State the blood parasite species.
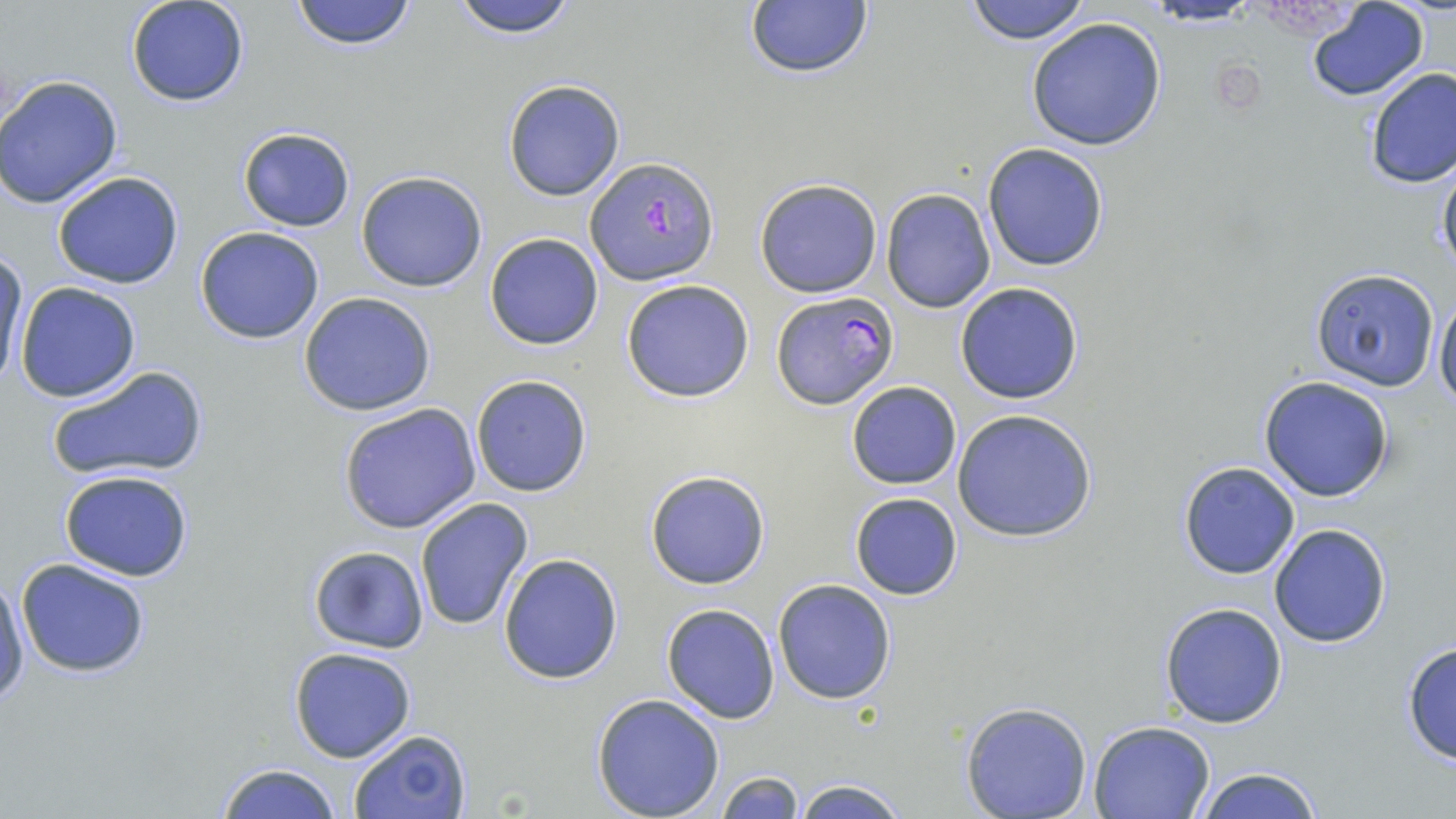
Plasmodium falciparum.

stain = May-Grünwald-Giemsa
uninfected red blood cell locations = approximate bounding boxes as (x1, y1, x2, y2) in pixels: (125, 0, 252, 108), (291, 0, 418, 51), (448, 0, 581, 39), (962, 0, 1093, 45), (742, 2, 874, 81), (1304, 2, 1429, 101), (1025, 17, 1168, 152), (1361, 66, 1455, 191), (0, 74, 124, 210), (502, 80, 627, 202), (238, 126, 356, 232), (982, 143, 1110, 270), (1436, 158, 1456, 282), (52, 170, 185, 290), (356, 170, 488, 293), (754, 178, 883, 298), (881, 189, 996, 312), (193, 226, 325, 345), (484, 233, 604, 351), (1, 253, 28, 387), (1310, 269, 1441, 392), (621, 279, 756, 404), (955, 281, 1086, 404), (15, 282, 143, 403), (1433, 290, 1456, 411), (298, 291, 437, 417), (46, 363, 211, 483), (470, 374, 594, 497), (1258, 376, 1396, 502), (845, 381, 962, 489), (337, 403, 483, 535), (950, 408, 1100, 543), (1178, 461, 1300, 578), (58, 469, 194, 582), (644, 469, 771, 590), (848, 492, 964, 601), (414, 497, 534, 633), (1268, 523, 1393, 648), (308, 545, 430, 652), (498, 553, 623, 684), (15, 559, 151, 677), (1, 571, 29, 712), (771, 578, 896, 705), (1159, 601, 1288, 728), (661, 603, 780, 723), (1400, 640, 1456, 765), (288, 646, 417, 764), (591, 693, 724, 819), (959, 700, 1093, 819), (1087, 720, 1216, 819), (348, 729, 472, 819), (214, 764, 344, 819), (1190, 765, 1325, 819), (715, 770, 805, 818), (791, 777, 909, 818)
field of view = single
preparation = thin blood smear
modality = light microscopy
Plasmodium falciparum-infected red blood cell locations = approximate bounding boxes as (x1, y1, x2, y2) in pixels: (586, 157, 719, 285), (772, 290, 898, 410)
magnification = 1000x
image size = 1456×819 pixels